Locate every malaria parasite.
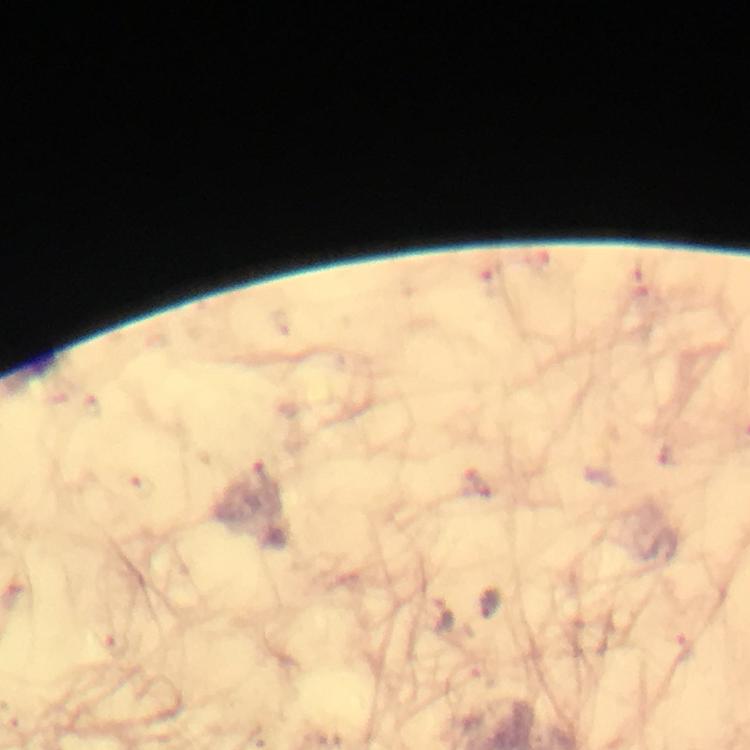
Approximate centers as {x, y} in pixels.
Malaria parasites: {267, 470}, {490, 604}, {442, 616}.

capture: smartphone photograph through a microscope
cropped_from: one field of view
stain: Giemsa
image_size: 750×750 pixels
immersion_oil: applied
context: from a diagnostic examination for malaria
magnification: 100x
preparation: thick blood smear